State which parasite is depicted.
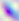

This is Toxoplasma gondii.

Summary:
  - Modality: micrograph
  - Magnification: 400x